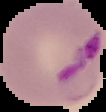

result = Plasmodium parasites detected
image size = 106×112 pixels
image type = segmented cell region on a black background
preparation = thin blood film